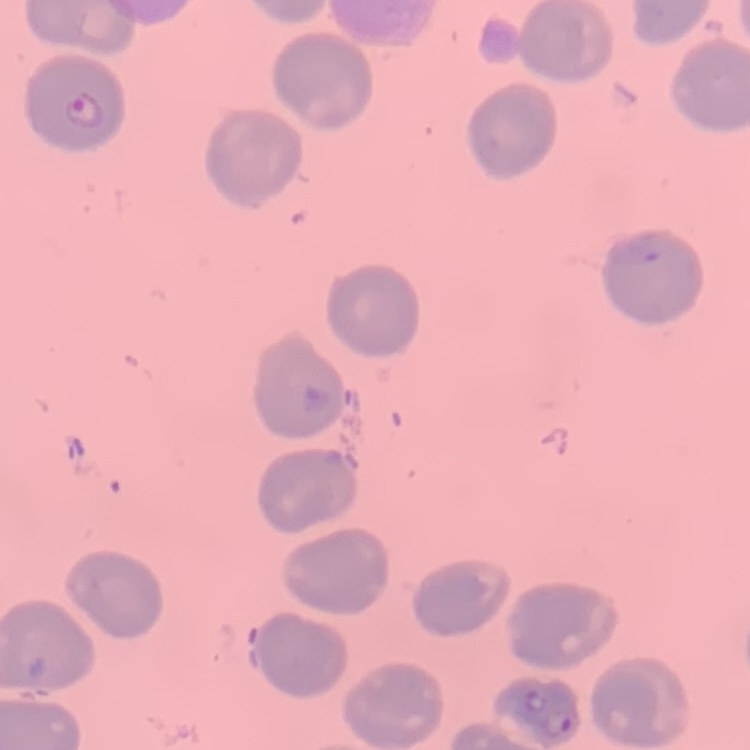

Summary:
  - Red blood cell morphology: no rouleaux formation
  - Preparation: thin blood smear
  - Stain: Field's or Giemsa
  - Image type: one tile cut from a larger photomicrograph